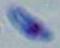

1000x magnification. Toxoplasma gondii is seen. Micrograph.